Assess this cell for malaria.
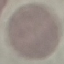

Uninfected.

Summary:
  - Capture: smartphone camera at the microscope eyepiece
  - Stain: Giemsa
  - Preparation: thin smear
  - Image type: automatically extracted cell patch, resized to 64 × 64 pixels